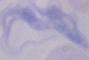

modality: micrograph
identification: trypanosome
magnification: 1000x